Give the extent of all Plasmodium falciparum-infected red blood cells.
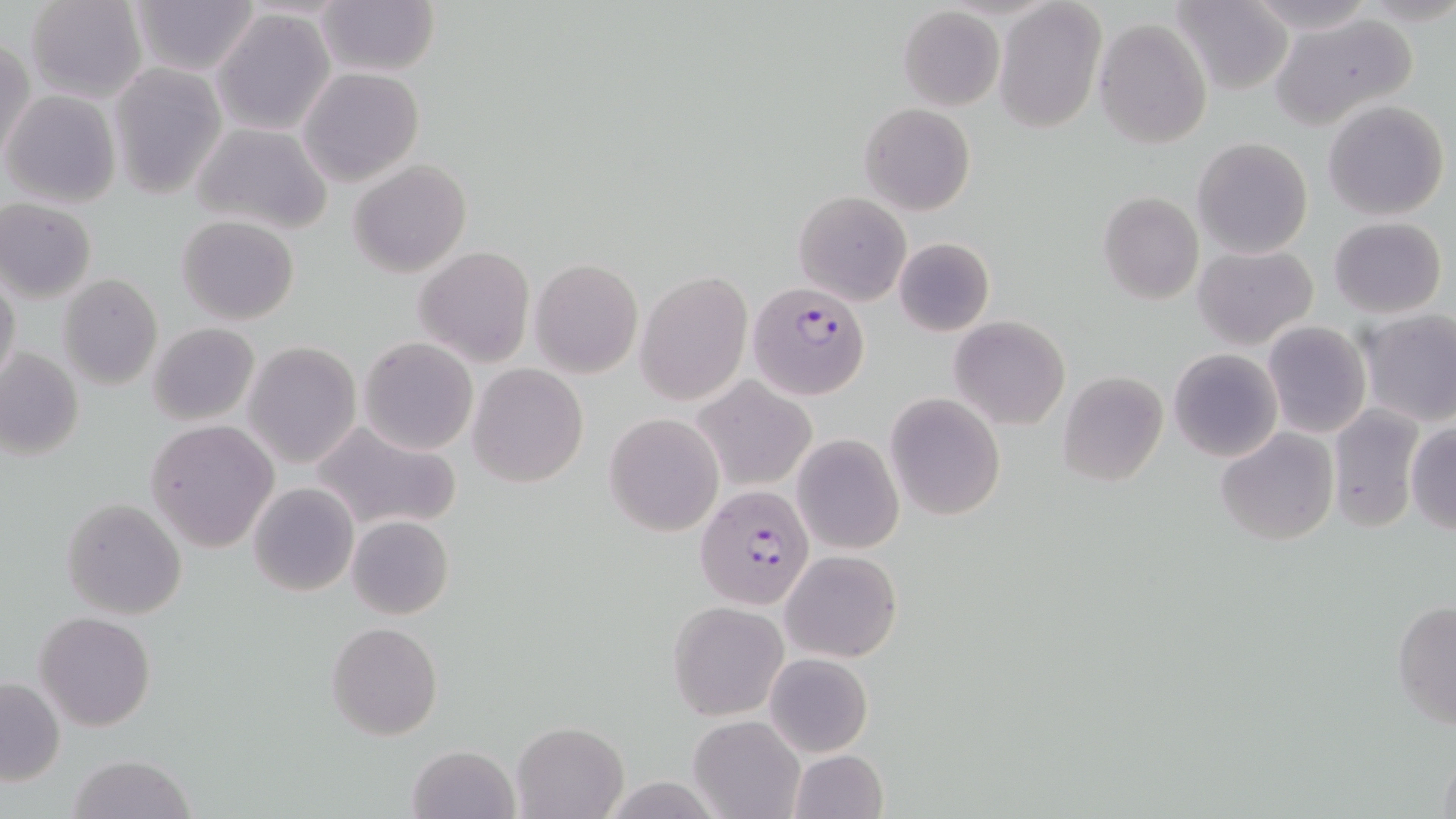
Approximate bounding boxes as [x1, y1, x2, y2] in pixels.
Plasmodium falciparum-infected red blood cells: [745, 281, 870, 400], [696, 483, 817, 609].

Uninfected red blood cell locations: [24, 0, 148, 104], [128, 0, 261, 75], [1241, 0, 1378, 36], [994, 1, 1107, 135], [1171, 1, 1295, 95], [313, 2, 439, 78], [898, 6, 1005, 111], [212, 7, 337, 137], [1270, 12, 1418, 132], [1093, 17, 1213, 150], [1, 36, 35, 165], [109, 64, 227, 200], [298, 67, 423, 186], [4, 91, 121, 208], [241, 91, 407, 217], [1322, 99, 1450, 221], [860, 103, 976, 216], [191, 121, 333, 235], [1192, 136, 1312, 258], [349, 159, 471, 277], [793, 190, 911, 306], [1098, 191, 1203, 305], [1, 198, 98, 301], [177, 215, 301, 325], [1328, 217, 1447, 318], [893, 236, 994, 336], [1193, 245, 1318, 348], [416, 246, 534, 367], [530, 256, 642, 379], [0, 272, 22, 391], [636, 272, 752, 405], [58, 274, 163, 390], [1359, 311, 1456, 428], [950, 316, 1070, 429], [1262, 321, 1371, 437], [146, 323, 260, 425], [358, 337, 479, 455], [244, 342, 360, 468], [1, 347, 84, 460], [1168, 347, 1283, 463], [468, 364, 588, 488], [1056, 371, 1168, 487], [692, 378, 816, 491], [885, 392, 1004, 520], [1326, 403, 1425, 532], [605, 412, 723, 536], [143, 419, 279, 553], [310, 420, 463, 533], [1405, 421, 1456, 535], [1216, 429, 1339, 546], [791, 432, 903, 555], [247, 482, 359, 598], [61, 498, 187, 619], [347, 515, 454, 621], [780, 548, 902, 663], [1391, 598, 1456, 729], [667, 600, 788, 721], [34, 610, 157, 731], [327, 620, 443, 741], [763, 652, 873, 759], [0, 676, 65, 785], [687, 715, 804, 819], [511, 720, 628, 818], [408, 743, 518, 818], [1436, 744, 1456, 819], [786, 750, 887, 819], [68, 754, 196, 819]. Slide-level diagnosis: Plasmodium falciparum. 1000x magnification. Optical microscopy. One field of a larger specimen. Image is 1456×819 pixels. Thin blood film. May-Grünwald-Giemsa-stained preparation.